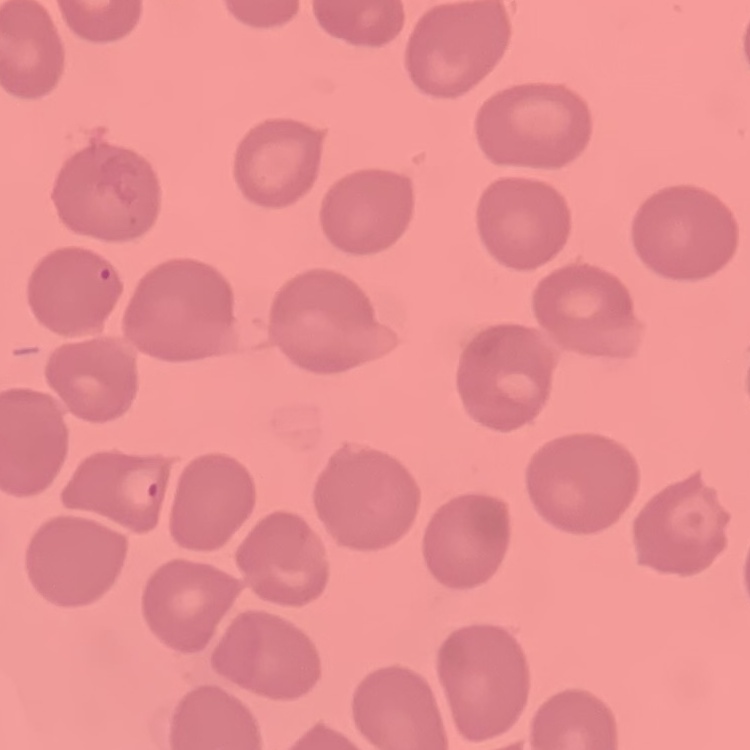
Summary:
  - Erythrocyte morphology: no rouleaux formation
  - Preparation: thin blood film
  - Image type: one tile cut from a larger photomicrograph
  - Stain: Field's or Giemsa